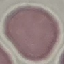
Summary:
  - Result: negative for malaria parasites
  - Preparation: thin smear
  - Capture: smartphone camera at the microscope eyepiece
  - Stain: Giemsa
  - Image type: automatically extracted cell patch, resized to 64 × 64 pixels